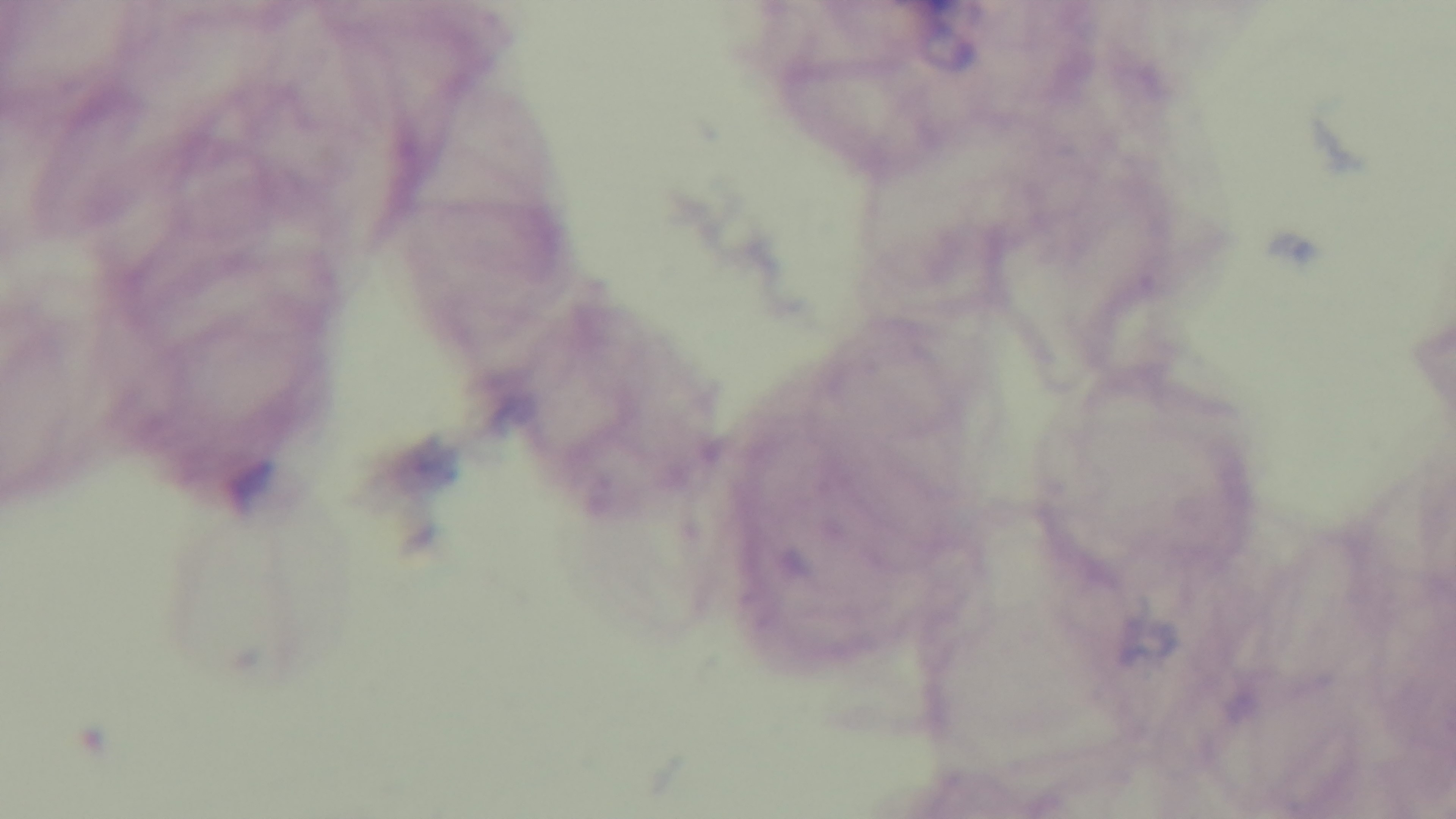
objective = 100x oil immersion
stain = Giemsa
field of view = one from the slide
preparation = thick smear
malaria status = uninfected
modality = light microscopy
capture = mounted 4K digital camera